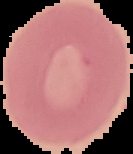
Image is 133×154 pixels. From a thin blood smear. Malaria status: uninfected. Segmented cell region on a black background.